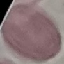

Summary:
  - Malaria status: uninfected
  - Preparation: thin blood smear
  - Capture: smartphone camera at the microscope eyepiece
  - Image type: cell patch, automatically extracted from a larger field of view and resized to 64 × 64 pixels
  - Stain: Giemsa